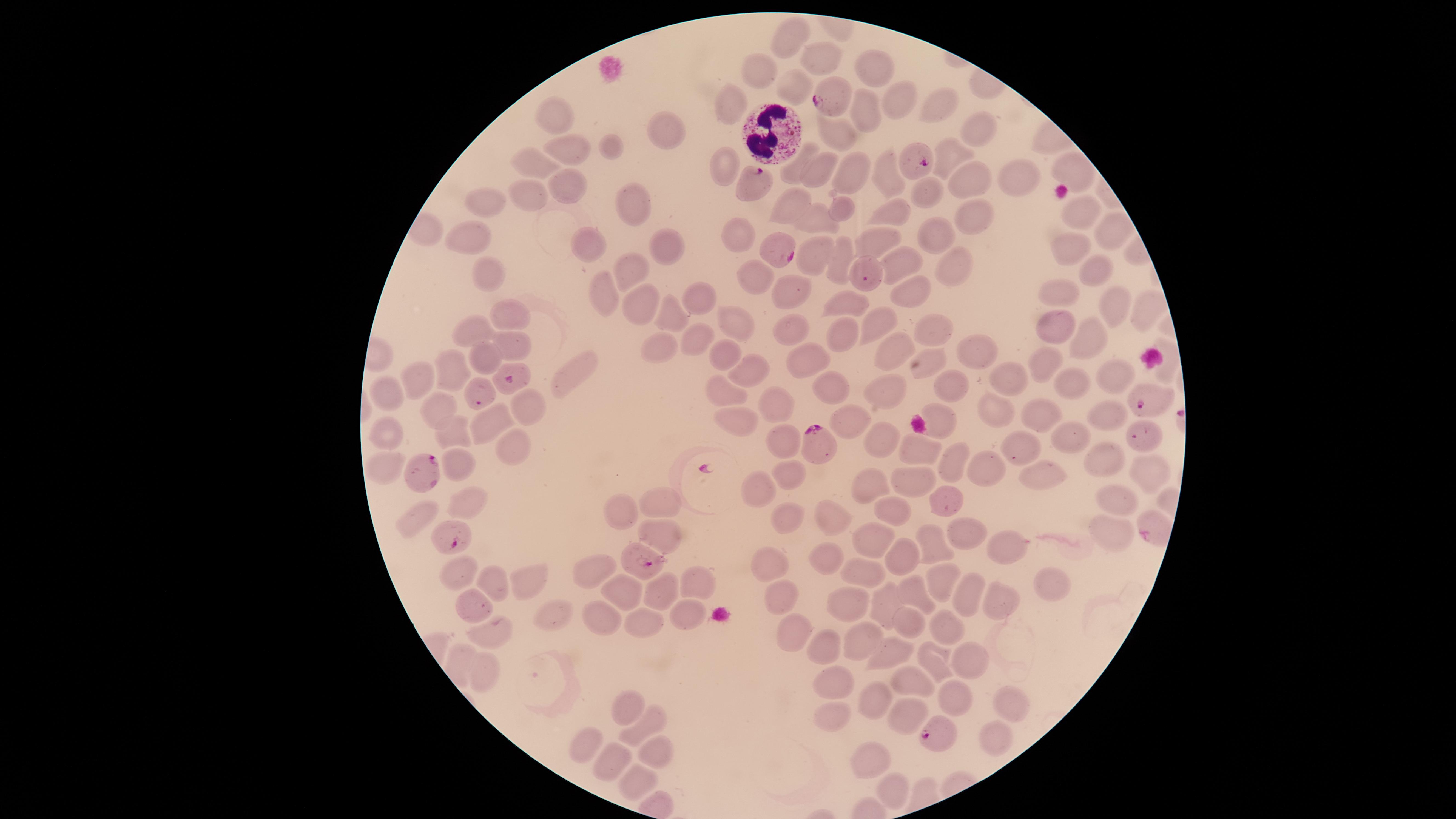

Approximate marker points as (x, y) in pixels. Parasitized RBCs: (834, 92), (919, 163), (752, 181), (781, 249), (514, 382), (1147, 401), (821, 443), (423, 471), (1157, 530), (444, 535), (643, 562), (937, 731). WBCs: (769, 129). Uninfected RBCs: (792, 35), (818, 53), (870, 61), (759, 71), (790, 82), (894, 99), (931, 101), (732, 102), (861, 110), (558, 114), (661, 128), (973, 128), (839, 134), (576, 146), (618, 148), (952, 152), (541, 159), (725, 164), (792, 165), (821, 168), (1071, 170), (885, 172), (854, 176), (960, 177), (1018, 180), (569, 183), (532, 192), (927, 193), (486, 196), (791, 203), (629, 204), (840, 204), (1076, 209), (895, 211), (967, 212), (818, 217), (1108, 227), (469, 232), (737, 234), (935, 234), (878, 235), (592, 246), (662, 247), (1064, 248), (845, 252), (811, 257), (901, 258), (949, 266), (1094, 267), (629, 269), (483, 275), (748, 280), (797, 287), (908, 290), (1055, 290), (607, 291), (641, 297), (697, 297), (844, 299), (1113, 305), (1144, 307), (672, 312), (510, 315), (877, 321), (737, 322), (929, 325), (474, 328), (1057, 328), (790, 329), (1088, 333), (693, 334), (850, 335), (895, 343), (510, 344), (662, 349), (979, 351), (721, 354), (486, 355), (799, 360), (931, 361), (1055, 365), (750, 370), (451, 372), (568, 374), (1116, 374), (1006, 377), (422, 379), (1073, 381), (949, 385), (831, 388), (387, 390), (881, 392), (726, 393), (768, 399), (443, 406), (993, 409), (1103, 409), (528, 410), (1042, 413), (846, 417), (741, 418), (492, 423), (940, 426), (389, 430), (449, 432), (885, 437), (1059, 437), (782, 438), (1017, 444), (515, 446), (917, 449), (1100, 458), (952, 460), (383, 463), (454, 465), (993, 468), (791, 470), (1141, 471), (1046, 475), (915, 479), (867, 485), (763, 490), (657, 498), (946, 498), (471, 500), (1119, 504), (893, 506), (619, 512), (836, 515), (783, 516), (417, 523), (1113, 534), (665, 535), (869, 535), (968, 539), (929, 543), (1003, 544), (895, 555), (830, 559), (588, 567), (768, 568), (458, 574), (860, 574), (939, 574), (528, 580), (497, 581), (701, 584), (1052, 584), (914, 589), (663, 590), (624, 591), (773, 594), (967, 596), (998, 599), (469, 603), (842, 604), (884, 606), (560, 613), (687, 615), (599, 616), (942, 623), (647, 624), (908, 627), (790, 629), (480, 632), (858, 639), (828, 647), (886, 649), (962, 658), (934, 662), (476, 666), (909, 680), (836, 681), (946, 692), (1005, 697), (876, 700), (625, 705), (900, 710), (833, 713), (642, 730), (992, 740), (583, 748), (655, 752), (873, 760), (602, 768), (633, 785), (892, 795). Species: Plasmodium falciparum. One field of view of the specimen. Image is 1456×819 pixels. Smartphone photograph through the microscope eyepiece. Thin blood film. Presence: malaria parasites detected. Giemsa-stained preparation. The visible region is circular.